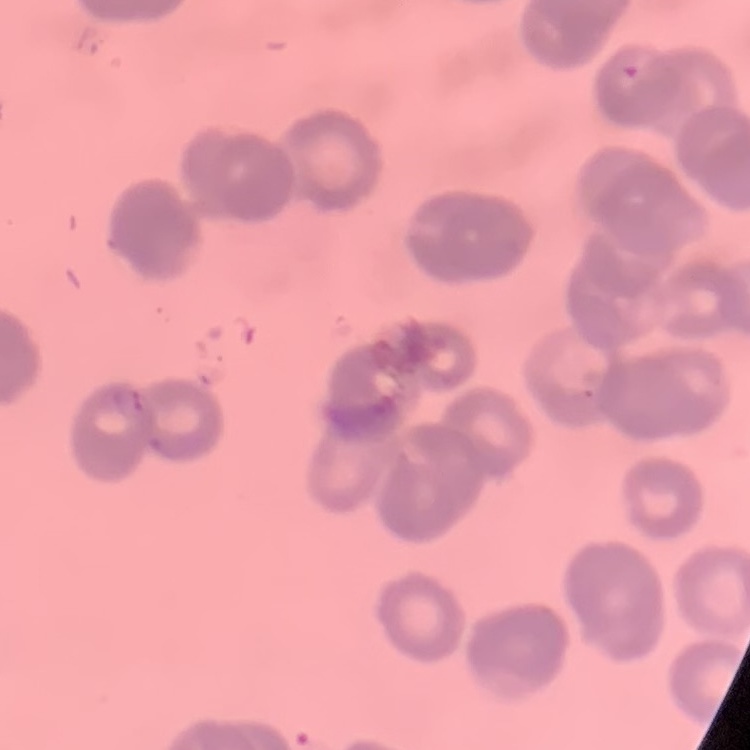

Summary:
  - Erythrocyte morphology: rouleaux formation
  - Image type: one tile cut from a larger photomicrograph
  - Preparation: thin blood film
  - Stain: Field's or Giemsa